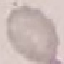
{
  "malaria_status": "uninfected",
  "preparation": "thin blood smear",
  "image_type": "cell patch, automatically extracted from a larger field of view and resized to 64 × 64 pixels",
  "capture": "smartphone through the microscope eyepiece",
  "stain": "Giemsa"
}